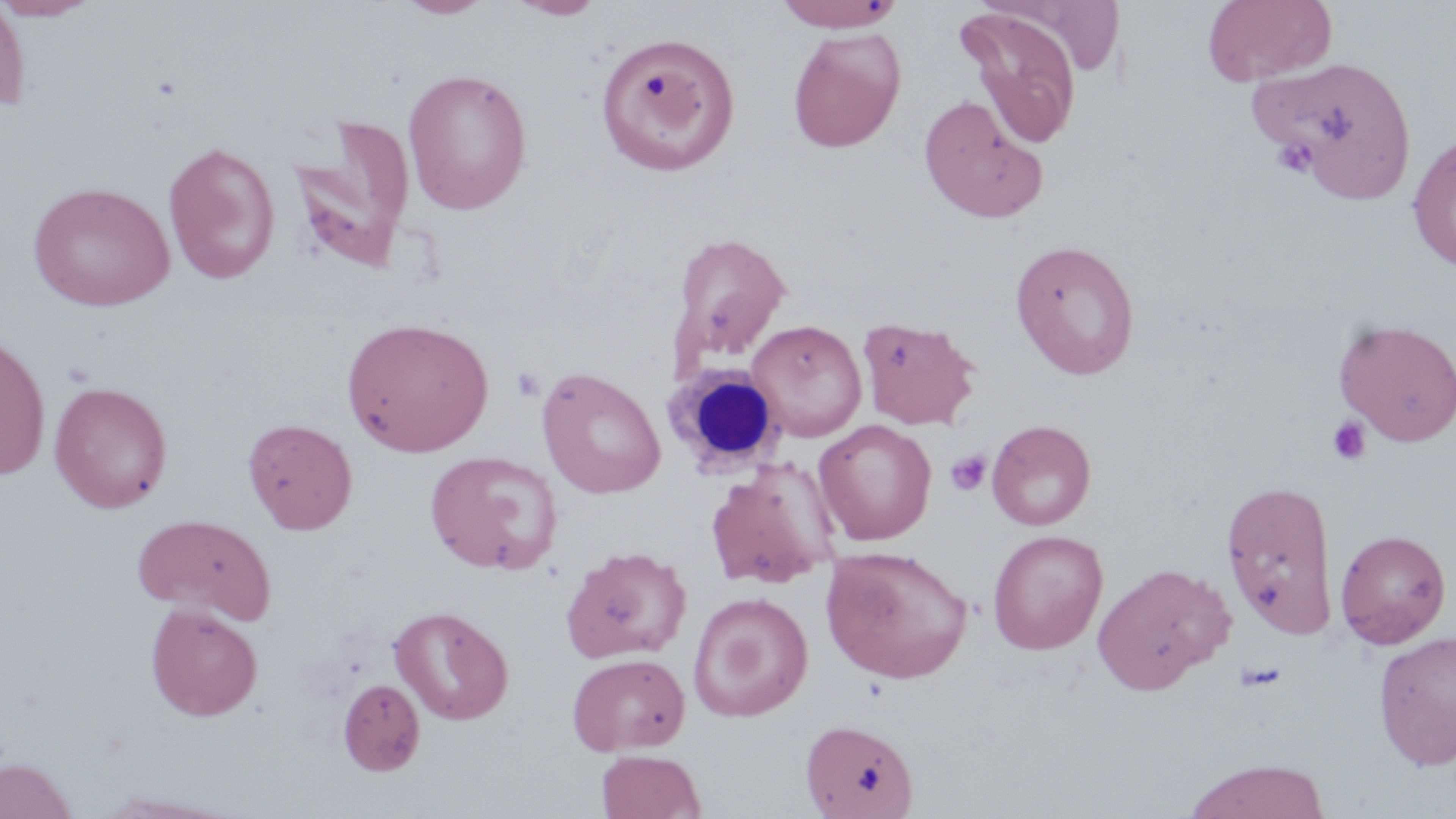
Summary:
  - Coordinate format: approximate bounding boxes as named x1/y1/x2/y2 corners in pixels
  - Uninfected red blood cell locations: (x1=0, y1=0, x2=100, y2=21), (x1=0, y1=0, x2=32, y2=112), (x1=396, y1=0, x2=495, y2=19), (x1=507, y1=0, x2=607, y2=20), (x1=771, y1=0, x2=907, y2=32), (x1=1203, y1=0, x2=1337, y2=85), (x1=957, y1=7, x2=1084, y2=148), (x1=788, y1=28, x2=906, y2=152), (x1=594, y1=33, x2=741, y2=176), (x1=1264, y1=56, x2=1419, y2=198), (x1=402, y1=67, x2=533, y2=214), (x1=918, y1=93, x2=1049, y2=223), (x1=288, y1=115, x2=416, y2=273), (x1=1407, y1=134, x2=1456, y2=272), (x1=163, y1=141, x2=281, y2=284), (x1=28, y1=181, x2=176, y2=311), (x1=670, y1=232, x2=792, y2=368), (x1=1009, y1=239, x2=1141, y2=379), (x1=857, y1=315, x2=981, y2=430), (x1=341, y1=316, x2=494, y2=457), (x1=1333, y1=318, x2=1456, y2=446), (x1=746, y1=319, x2=868, y2=442), (x1=0, y1=331, x2=51, y2=482), (x1=537, y1=367, x2=666, y2=499), (x1=49, y1=381, x2=173, y2=513), (x1=242, y1=417, x2=358, y2=534), (x1=814, y1=419, x2=937, y2=544), (x1=987, y1=419, x2=1096, y2=530), (x1=424, y1=449, x2=564, y2=575), (x1=703, y1=458, x2=839, y2=590), (x1=1220, y1=478, x2=1339, y2=640), (x1=131, y1=513, x2=278, y2=624), (x1=1335, y1=528, x2=1451, y2=649), (x1=987, y1=529, x2=1108, y2=655), (x1=560, y1=545, x2=692, y2=664), (x1=820, y1=545, x2=973, y2=684), (x1=1092, y1=561, x2=1233, y2=693), (x1=687, y1=591, x2=813, y2=722), (x1=145, y1=602, x2=263, y2=721), (x1=388, y1=605, x2=514, y2=726), (x1=1373, y1=631, x2=1456, y2=770), (x1=566, y1=652, x2=690, y2=755), (x1=337, y1=678, x2=425, y2=776), (x1=799, y1=718, x2=919, y2=818), (x1=596, y1=749, x2=706, y2=819), (x1=0, y1=756, x2=78, y2=819), (x1=1183, y1=758, x2=1330, y2=819)
  - Platelet locations: (x1=1273, y1=135, x2=1318, y2=179), (x1=511, y1=368, x2=546, y2=402), (x1=1327, y1=416, x2=1372, y2=466), (x1=946, y1=450, x2=992, y2=495)
  - White blood cell locations: (x1=668, y1=363, x2=790, y2=475)
  - Slide-level diagnosis: negative for blood parasites
  - Stain: May-Grünwald-Giemsa
  - Modality: optical microscopy
  - Field of view: one of a larger specimen
  - Preparation: thin blood smear
  - Image size: 1456×819 pixels
  - Magnification: 1000x